Report the malaria status of this cell.
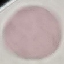

Uninfected.

Giemsa-stained preparation. Photographed with a smartphone camera at the microscope eyepiece. Automatically extracted cell patch, resized to 64 × 64 pixels. Thin blood smear.